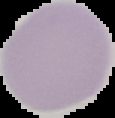

image_type: segmented cell region on a black background
image_size: 115×118 pixels
result: no Plasmodium parasites seen
preparation: thin blood film